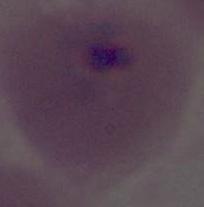 A Plasmodium parasite is seen. Micrograph. 400x or 1000x magnification.